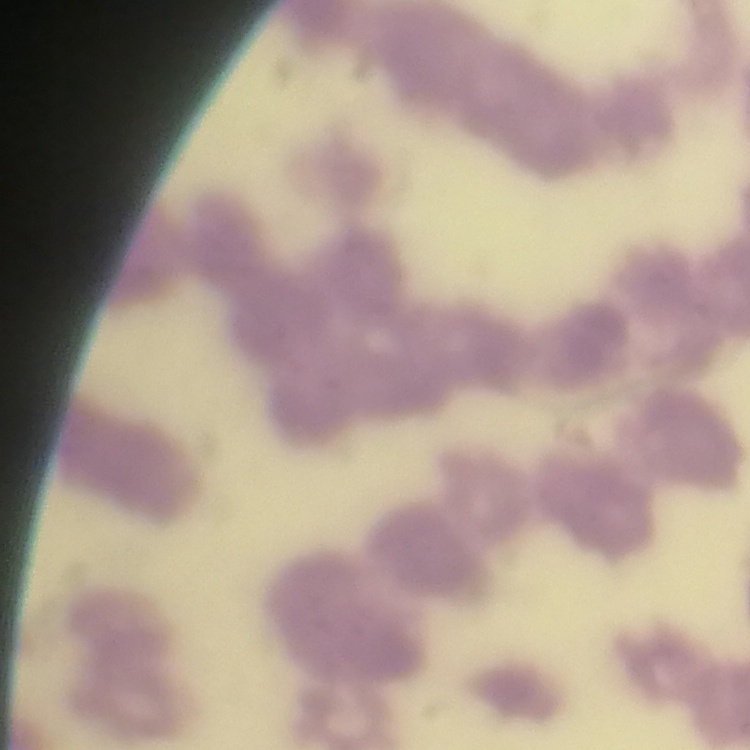 The erythrocytes exhibit rouleaux formation. Thin blood smear. One tile cut from a larger photomicrograph. Stained with either Field's or Giemsa.